Comment on the morphology of the red blood cells.
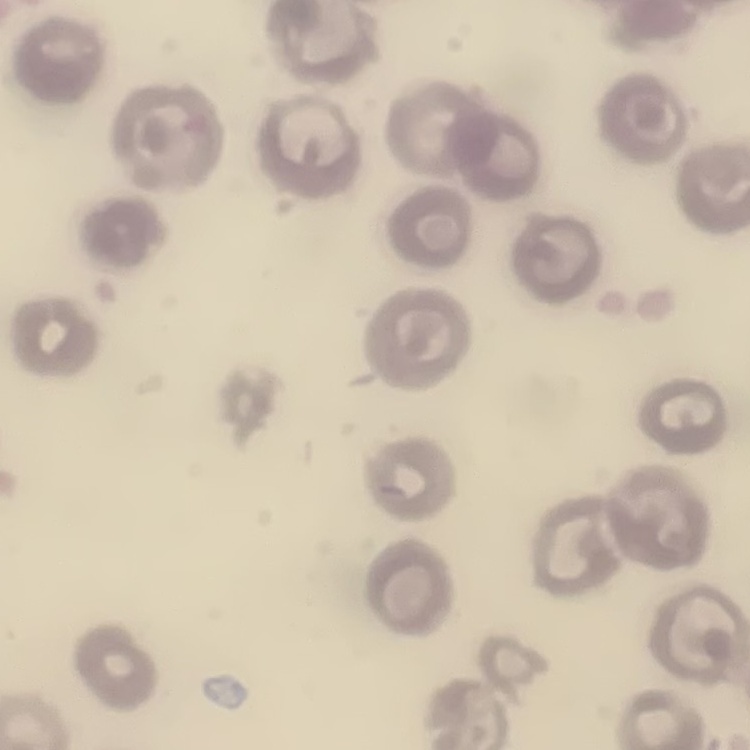

No rouleaux formation.

preparation: thin blood smear
image_type: square crop of a larger photomicrograph
stain: Field's or Giemsa